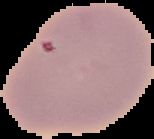
Summary:
  - Image type: segmented cell region on a black background
  - Result: no malaria parasites detected
  - Preparation: thin blood film
  - Image size: 154×139 pixels